Identify the parasite.
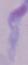

This is a trypanosome.

1000x magnification. Micrograph.